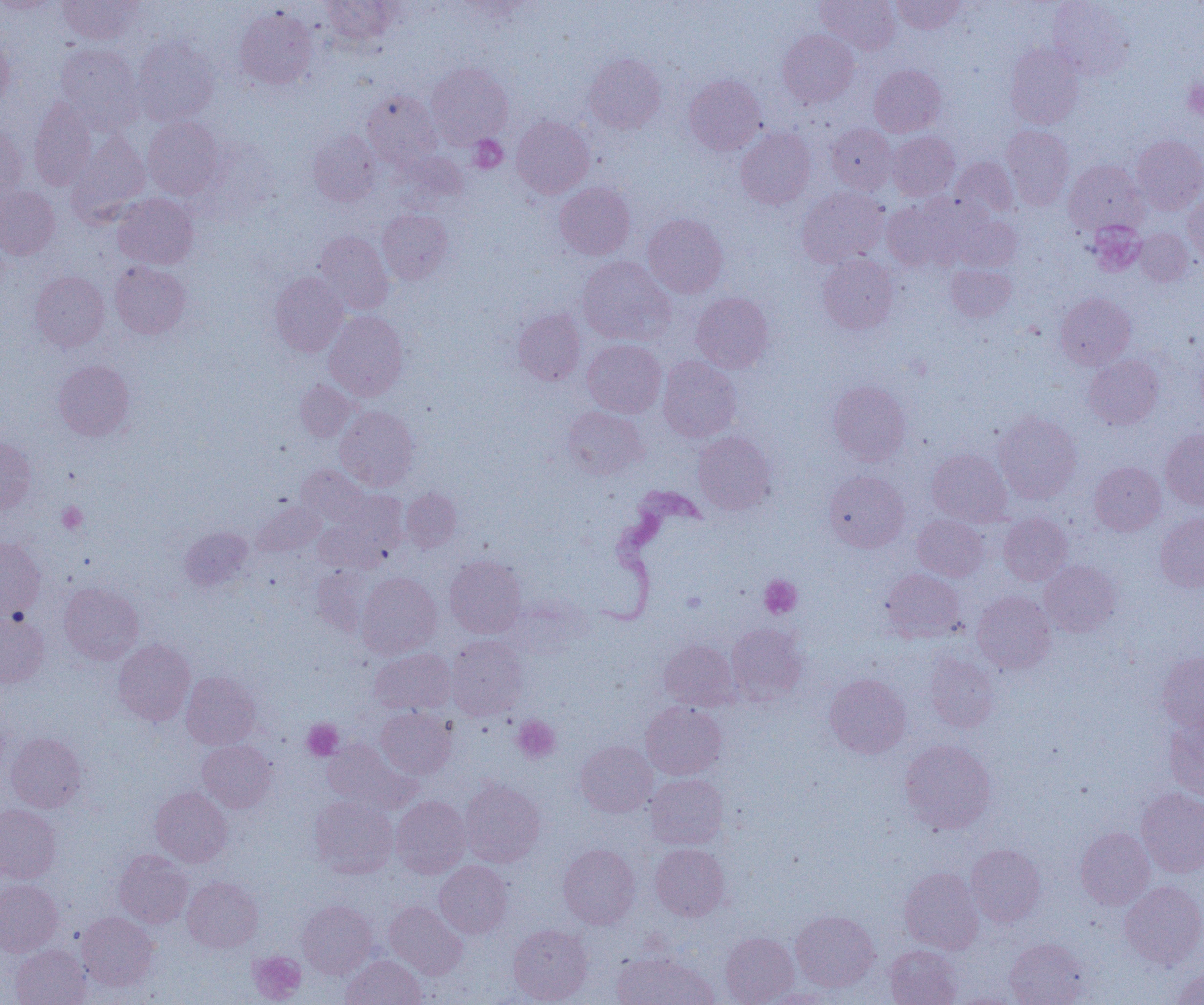

slide-level diagnosis = Trypanosoma brucei
preparation = thin blood smear
platelet locations = approximate bounding boxes as named x1/y1/x2/y2 corners in pixels: (x1=1183, y1=80, x2=1204, y2=120), (x1=469, y1=135, x2=507, y2=172), (x1=1088, y1=221, x2=1146, y2=276), (x1=57, y1=502, x2=88, y2=533), (x1=760, y1=575, x2=802, y2=618), (x1=512, y1=716, x2=560, y2=763), (x1=302, y1=719, x2=342, y2=761), (x1=248, y1=950, x2=306, y2=1003)
uninfected red blood cell locations = approximate bounding boxes as named x1/y1/x2/y2 corners in pixels: (x1=58, y1=0, x2=141, y2=44), (x1=322, y1=0, x2=398, y2=46), (x1=816, y1=0, x2=900, y2=55), (x1=891, y1=0, x2=965, y2=34), (x1=0, y1=1, x2=60, y2=14), (x1=1047, y1=1, x2=1134, y2=80), (x1=235, y1=7, x2=318, y2=89), (x1=778, y1=29, x2=859, y2=108), (x1=0, y1=36, x2=15, y2=111), (x1=133, y1=36, x2=219, y2=125), (x1=55, y1=43, x2=143, y2=128), (x1=1005, y1=43, x2=1085, y2=128), (x1=584, y1=53, x2=666, y2=133), (x1=426, y1=63, x2=512, y2=147), (x1=869, y1=65, x2=946, y2=137), (x1=684, y1=74, x2=766, y2=155), (x1=362, y1=91, x2=441, y2=168), (x1=29, y1=99, x2=97, y2=190), (x1=511, y1=115, x2=594, y2=198), (x1=143, y1=116, x2=224, y2=199), (x1=827, y1=123, x2=897, y2=194), (x1=0, y1=124, x2=27, y2=200), (x1=1001, y1=125, x2=1074, y2=210), (x1=736, y1=128, x2=815, y2=209), (x1=308, y1=130, x2=380, y2=206), (x1=888, y1=131, x2=960, y2=200), (x1=68, y1=132, x2=150, y2=221), (x1=1132, y1=135, x2=1204, y2=214), (x1=951, y1=157, x2=1019, y2=220), (x1=1064, y1=159, x2=1147, y2=235), (x1=555, y1=183, x2=635, y2=260), (x1=0, y1=185, x2=59, y2=259), (x1=797, y1=187, x2=889, y2=268), (x1=1183, y1=192, x2=1204, y2=266), (x1=112, y1=193, x2=198, y2=269), (x1=882, y1=198, x2=965, y2=271), (x1=377, y1=209, x2=453, y2=284), (x1=949, y1=211, x2=1022, y2=271), (x1=643, y1=214, x2=728, y2=297), (x1=1135, y1=228, x2=1193, y2=285), (x1=314, y1=232, x2=394, y2=314), (x1=817, y1=253, x2=898, y2=334), (x1=577, y1=256, x2=675, y2=344), (x1=110, y1=261, x2=190, y2=339), (x1=945, y1=264, x2=1016, y2=322), (x1=30, y1=271, x2=109, y2=352), (x1=270, y1=272, x2=348, y2=356), (x1=691, y1=292, x2=774, y2=373), (x1=1056, y1=292, x2=1135, y2=369), (x1=513, y1=309, x2=585, y2=385), (x1=324, y1=311, x2=408, y2=400), (x1=583, y1=339, x2=666, y2=417), (x1=1084, y1=354, x2=1163, y2=429), (x1=658, y1=356, x2=741, y2=442), (x1=54, y1=360, x2=134, y2=440), (x1=295, y1=380, x2=355, y2=442), (x1=828, y1=381, x2=911, y2=465), (x1=335, y1=406, x2=418, y2=491), (x1=562, y1=406, x2=648, y2=479), (x1=993, y1=411, x2=1082, y2=503), (x1=1161, y1=429, x2=1204, y2=509), (x1=693, y1=431, x2=776, y2=515), (x1=0, y1=438, x2=35, y2=514), (x1=927, y1=449, x2=1011, y2=526), (x1=1090, y1=461, x2=1165, y2=536), (x1=296, y1=465, x2=370, y2=526), (x1=824, y1=470, x2=909, y2=552), (x1=401, y1=488, x2=461, y2=552), (x1=318, y1=496, x2=407, y2=572), (x1=252, y1=500, x2=324, y2=556), (x1=1155, y1=512, x2=1204, y2=591), (x1=998, y1=513, x2=1072, y2=585), (x1=912, y1=514, x2=989, y2=581), (x1=180, y1=527, x2=253, y2=591), (x1=0, y1=537, x2=45, y2=618), (x1=445, y1=555, x2=527, y2=638), (x1=1039, y1=561, x2=1121, y2=636), (x1=311, y1=566, x2=375, y2=635), (x1=881, y1=569, x2=965, y2=642), (x1=356, y1=572, x2=441, y2=659), (x1=59, y1=583, x2=143, y2=664), (x1=972, y1=592, x2=1056, y2=674), (x1=0, y1=611, x2=50, y2=688), (x1=727, y1=623, x2=808, y2=704), (x1=445, y1=635, x2=528, y2=720), (x1=113, y1=639, x2=195, y2=725), (x1=659, y1=639, x2=740, y2=710), (x1=370, y1=648, x2=455, y2=715), (x1=1158, y1=652, x2=1204, y2=731), (x1=924, y1=653, x2=998, y2=732), (x1=181, y1=672, x2=260, y2=750), (x1=824, y1=674, x2=911, y2=758), (x1=641, y1=702, x2=726, y2=779), (x1=376, y1=707, x2=456, y2=779), (x1=1165, y1=715, x2=1204, y2=800), (x1=6, y1=733, x2=86, y2=813), (x1=322, y1=738, x2=418, y2=813), (x1=899, y1=739, x2=996, y2=834), (x1=198, y1=740, x2=276, y2=812), (x1=575, y1=741, x2=657, y2=817), (x1=646, y1=773, x2=728, y2=849), (x1=459, y1=779, x2=545, y2=866), (x1=151, y1=787, x2=232, y2=866), (x1=1136, y1=788, x2=1204, y2=877), (x1=310, y1=795, x2=398, y2=877), (x1=391, y1=796, x2=470, y2=878), (x1=0, y1=805, x2=60, y2=883), (x1=1076, y1=827, x2=1154, y2=909), (x1=650, y1=843, x2=730, y2=920), (x1=559, y1=844, x2=641, y2=929), (x1=966, y1=844, x2=1046, y2=927), (x1=114, y1=850, x2=192, y2=928), (x1=435, y1=861, x2=512, y2=938), (x1=900, y1=867, x2=984, y2=953), (x1=182, y1=877, x2=263, y2=952), (x1=0, y1=879, x2=62, y2=956), (x1=1120, y1=881, x2=1204, y2=968), (x1=298, y1=901, x2=376, y2=978), (x1=385, y1=901, x2=468, y2=979), (x1=791, y1=910, x2=880, y2=991), (x1=77, y1=912, x2=159, y2=991), (x1=508, y1=924, x2=593, y2=1004), (x1=720, y1=932, x2=798, y2=1005), (x1=1005, y1=938, x2=1089, y2=1005), (x1=11, y1=944, x2=90, y2=1005), (x1=884, y1=945, x2=962, y2=1005), (x1=612, y1=951, x2=717, y2=1005), (x1=341, y1=955, x2=425, y2=1005), (x1=1171, y1=966, x2=1204, y2=1005), (x1=757, y1=989, x2=839, y2=1004), (x1=947, y1=991, x2=1025, y2=1005)
magnification = 1000x
image size = 1204×1005 pixels
modality = optical microscopy
field of view = single
Trypanosoma brucei locations = approximate bounding boxes as named x1/y1/x2/y2 corners in pixels: (x1=599, y1=484, x2=707, y2=626)